Comment on the morphology of the red blood cells.
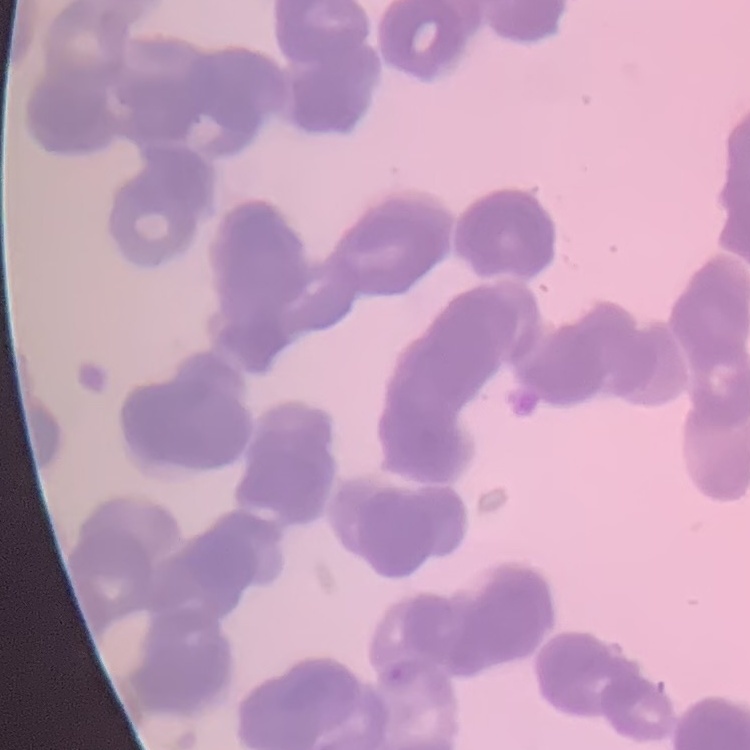
Rouleaux formation.

Summary:
  - Preparation: thin blood smear
  - Image type: one tile cut from a larger photomicrograph
  - Stain: Field's or Giemsa